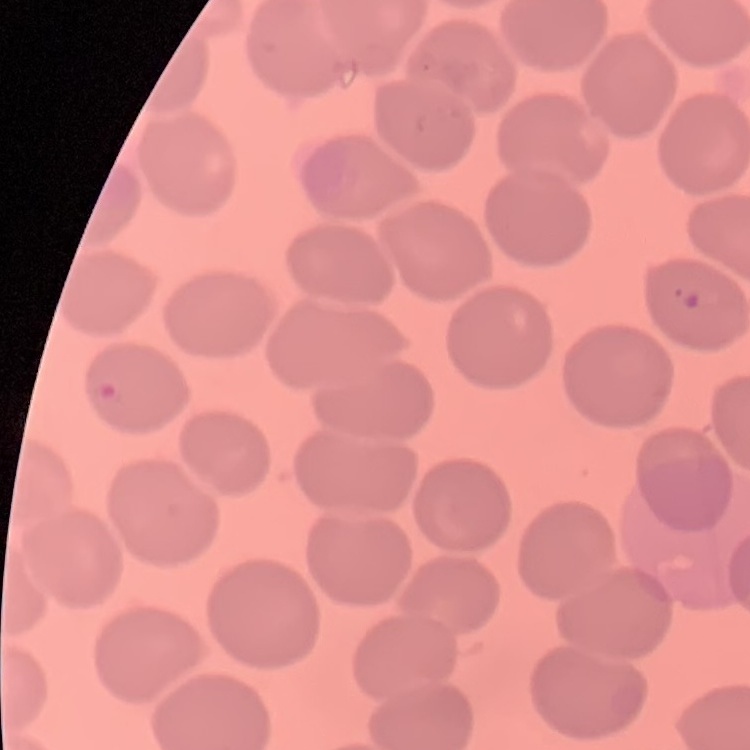

The red blood cells show no rouleaux formation. Field's or Giemsa stain. Square crop of a larger photomicrograph. Thin blood film.